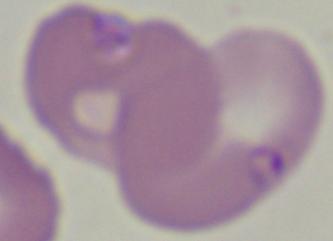

Summary:
  - Modality: micrograph
  - Identification: Babesia
  - Magnification: 1000x